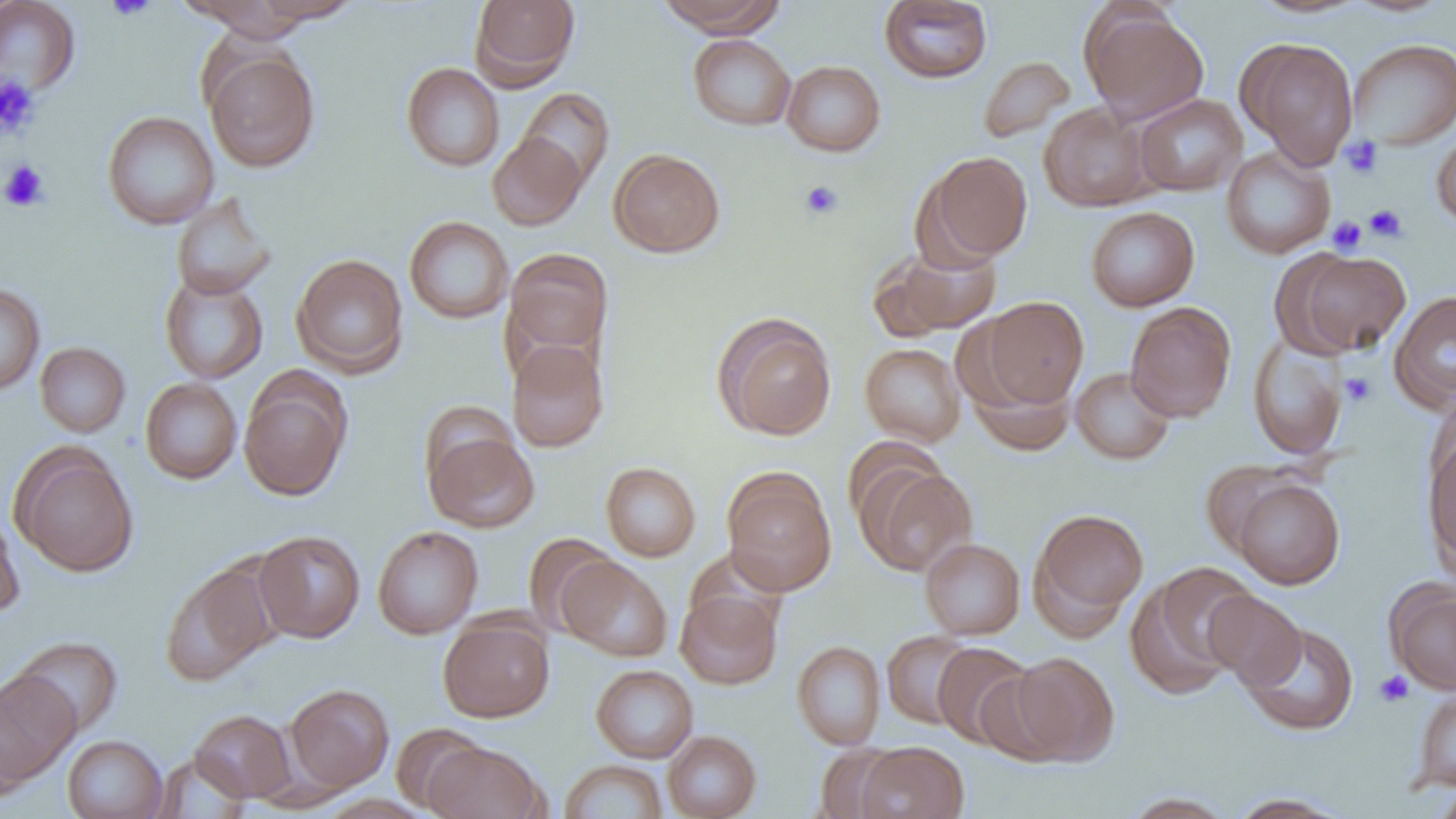
{
  "slide_level_diagnosis": "negative for blood parasites",
  "uninfected_red_blood_cell_locations": "approximate bounding boxes as named x1/y1/x2/y2 corners in pixels: (x1=252, y1=0, x2=363, y2=23), (x1=470, y1=0, x2=580, y2=88), (x1=656, y1=0, x2=785, y2=36), (x1=879, y1=0, x2=993, y2=84), (x1=1248, y1=0, x2=1369, y2=18), (x1=1343, y1=0, x2=1454, y2=17), (x1=0, y1=1, x2=81, y2=96), (x1=185, y1=1, x2=322, y2=40), (x1=1080, y1=5, x2=1209, y2=124), (x1=688, y1=34, x2=796, y2=130), (x1=1348, y1=38, x2=1455, y2=150), (x1=1240, y1=39, x2=1358, y2=168), (x1=203, y1=46, x2=320, y2=173), (x1=978, y1=56, x2=1076, y2=144), (x1=781, y1=60, x2=885, y2=156), (x1=402, y1=62, x2=505, y2=172), (x1=517, y1=87, x2=614, y2=188), (x1=1133, y1=94, x2=1247, y2=196), (x1=1039, y1=102, x2=1154, y2=212), (x1=102, y1=111, x2=219, y2=229), (x1=1431, y1=127, x2=1456, y2=229), (x1=488, y1=132, x2=588, y2=231), (x1=1221, y1=147, x2=1336, y2=258), (x1=608, y1=148, x2=725, y2=257), (x1=921, y1=151, x2=1033, y2=264), (x1=171, y1=193, x2=277, y2=300), (x1=1085, y1=206, x2=1200, y2=312), (x1=404, y1=216, x2=514, y2=324), (x1=872, y1=242, x2=1003, y2=340), (x1=504, y1=248, x2=614, y2=364), (x1=1286, y1=250, x2=1412, y2=356), (x1=292, y1=253, x2=409, y2=377), (x1=159, y1=272, x2=269, y2=384), (x1=0, y1=283, x2=45, y2=396), (x1=1389, y1=290, x2=1456, y2=411), (x1=982, y1=296, x2=1088, y2=407), (x1=1125, y1=301, x2=1236, y2=422), (x1=715, y1=315, x2=837, y2=441), (x1=1248, y1=336, x2=1348, y2=460), (x1=508, y1=341, x2=608, y2=452), (x1=35, y1=342, x2=130, y2=438), (x1=860, y1=343, x2=966, y2=446), (x1=966, y1=365, x2=1077, y2=455), (x1=1071, y1=367, x2=1176, y2=465), (x1=239, y1=376, x2=351, y2=500), (x1=140, y1=378, x2=242, y2=484), (x1=417, y1=399, x2=519, y2=490), (x1=424, y1=429, x2=539, y2=533), (x1=1422, y1=431, x2=1456, y2=570), (x1=13, y1=447, x2=139, y2=577), (x1=1199, y1=460, x2=1307, y2=555), (x1=601, y1=461, x2=700, y2=562), (x1=859, y1=463, x2=977, y2=576), (x1=722, y1=470, x2=837, y2=596), (x1=1231, y1=478, x2=1344, y2=589), (x1=1031, y1=507, x2=1148, y2=629), (x1=0, y1=511, x2=25, y2=619), (x1=372, y1=526, x2=483, y2=639), (x1=253, y1=530, x2=365, y2=643), (x1=523, y1=533, x2=620, y2=636), (x1=920, y1=538, x2=1025, y2=639), (x1=557, y1=557, x2=673, y2=662), (x1=161, y1=561, x2=278, y2=686), (x1=1129, y1=563, x2=1259, y2=697), (x1=1386, y1=582, x2=1456, y2=693), (x1=675, y1=588, x2=783, y2=690), (x1=1205, y1=590, x2=1308, y2=691), (x1=438, y1=614, x2=555, y2=722), (x1=1241, y1=623, x2=1359, y2=735), (x1=881, y1=630, x2=977, y2=730), (x1=10, y1=635, x2=124, y2=737), (x1=792, y1=640, x2=886, y2=750), (x1=932, y1=642, x2=1035, y2=749), (x1=1007, y1=651, x2=1120, y2=765), (x1=591, y1=664, x2=698, y2=763), (x1=974, y1=669, x2=1070, y2=766), (x1=0, y1=670, x2=80, y2=787), (x1=283, y1=683, x2=394, y2=793), (x1=1415, y1=688, x2=1456, y2=792), (x1=1, y1=708, x2=30, y2=808), (x1=190, y1=709, x2=297, y2=803), (x1=390, y1=723, x2=486, y2=813), (x1=662, y1=730, x2=761, y2=819), (x1=62, y1=735, x2=169, y2=819), (x1=423, y1=741, x2=545, y2=819), (x1=854, y1=741, x2=969, y2=819), (x1=813, y1=744, x2=905, y2=819), (x1=150, y1=753, x2=252, y2=818), (x1=559, y1=760, x2=668, y2=818), (x1=1432, y1=784, x2=1456, y2=819), (x1=1120, y1=792, x2=1236, y2=818), (x1=1225, y1=792, x2=1354, y2=818), (x1=317, y1=794, x2=435, y2=819)",
  "platelet_locations": "approximate bounding boxes as named x1/y1/x2/y2 corners in pixels: (x1=104, y1=0, x2=157, y2=21), (x1=0, y1=76, x2=40, y2=139), (x1=1340, y1=136, x2=1383, y2=179), (x1=1, y1=160, x2=48, y2=212), (x1=799, y1=180, x2=844, y2=220), (x1=1365, y1=204, x2=1408, y2=242), (x1=1327, y1=216, x2=1367, y2=255), (x1=1340, y1=373, x2=1376, y2=406), (x1=1375, y1=671, x2=1415, y2=706)",
  "field_of_view": "single",
  "magnification": "1000x",
  "modality": "light microscopy",
  "preparation": "thin blood smear",
  "image_size": "1456×819 pixels"
}